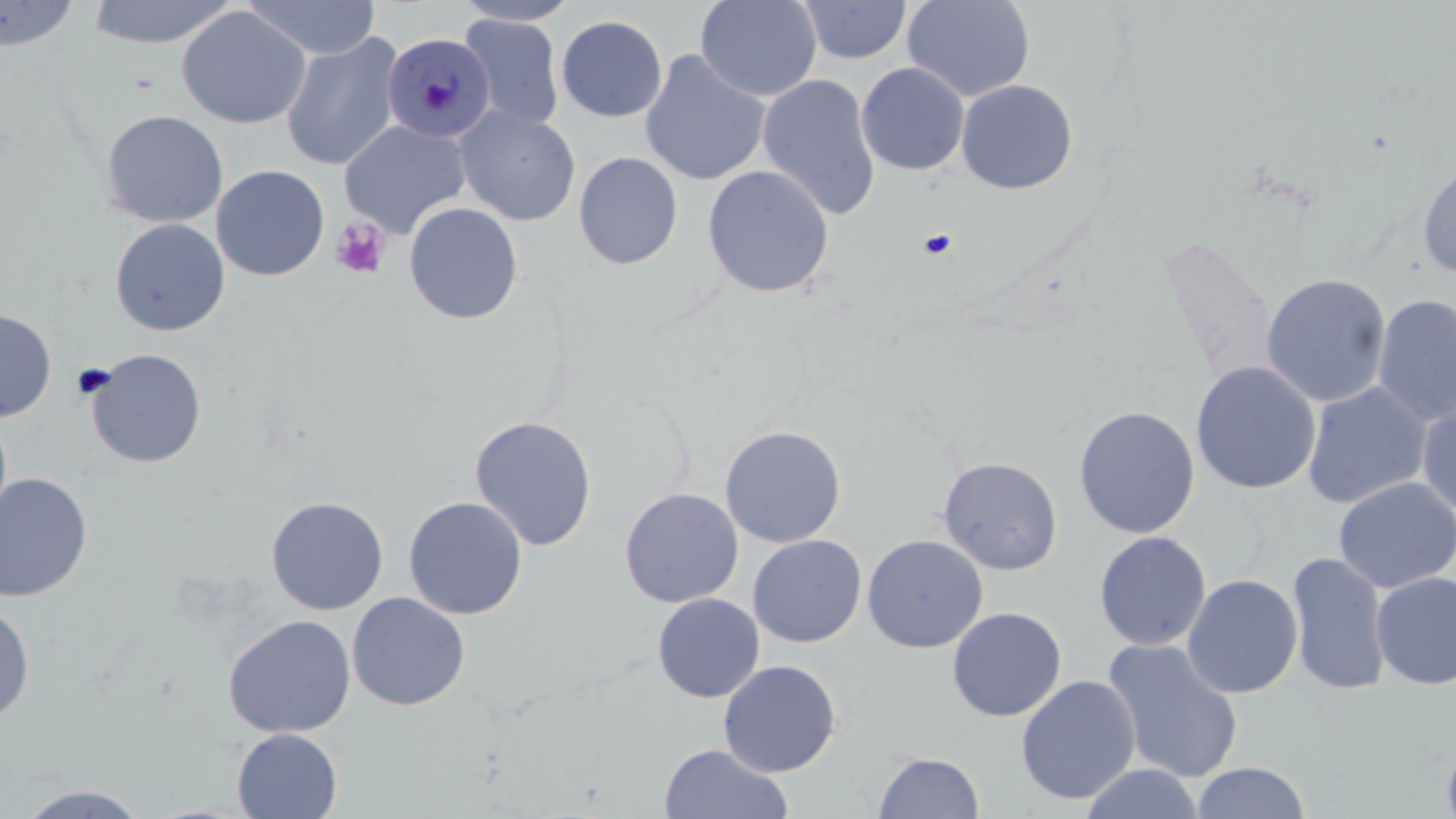
slide-level diagnosis = Plasmodium malariae
uninfected red blood cell locations = approximate bounding boxes as named x1/y1/x2/y2 corners in pixels: (x1=85, y1=0, x2=238, y2=48), (x1=243, y1=0, x2=381, y2=60), (x1=694, y1=0, x2=822, y2=102), (x1=903, y1=0, x2=1035, y2=103), (x1=0, y1=1, x2=81, y2=52), (x1=452, y1=1, x2=581, y2=26), (x1=799, y1=1, x2=912, y2=64), (x1=176, y1=6, x2=311, y2=129), (x1=459, y1=14, x2=566, y2=132), (x1=555, y1=14, x2=668, y2=123), (x1=280, y1=31, x2=404, y2=171), (x1=639, y1=49, x2=770, y2=186), (x1=856, y1=62, x2=970, y2=176), (x1=757, y1=73, x2=881, y2=221), (x1=956, y1=79, x2=1078, y2=195), (x1=455, y1=106, x2=580, y2=226), (x1=99, y1=109, x2=228, y2=228), (x1=338, y1=119, x2=471, y2=238), (x1=573, y1=151, x2=683, y2=270), (x1=1417, y1=155, x2=1456, y2=279), (x1=211, y1=164, x2=330, y2=281), (x1=702, y1=164, x2=835, y2=298), (x1=403, y1=201, x2=523, y2=325), (x1=109, y1=217, x2=230, y2=336), (x1=1155, y1=235, x2=1277, y2=383), (x1=1261, y1=273, x2=1392, y2=408), (x1=1372, y1=293, x2=1456, y2=427), (x1=0, y1=308, x2=56, y2=422), (x1=85, y1=348, x2=207, y2=468), (x1=1190, y1=360, x2=1322, y2=495), (x1=1301, y1=381, x2=1432, y2=509), (x1=1416, y1=397, x2=1456, y2=517), (x1=1073, y1=405, x2=1200, y2=538), (x1=0, y1=408, x2=13, y2=531), (x1=469, y1=415, x2=598, y2=551), (x1=719, y1=424, x2=846, y2=548), (x1=938, y1=456, x2=1063, y2=575), (x1=0, y1=472, x2=93, y2=602), (x1=1333, y1=477, x2=1456, y2=593), (x1=619, y1=487, x2=743, y2=608), (x1=266, y1=496, x2=389, y2=615), (x1=403, y1=496, x2=528, y2=619), (x1=1093, y1=530, x2=1211, y2=651), (x1=747, y1=534, x2=867, y2=648), (x1=862, y1=534, x2=989, y2=653), (x1=1287, y1=551, x2=1392, y2=695), (x1=1371, y1=571, x2=1456, y2=690), (x1=1181, y1=573, x2=1303, y2=699), (x1=347, y1=592, x2=470, y2=710), (x1=652, y1=593, x2=764, y2=703), (x1=1, y1=600, x2=35, y2=726), (x1=946, y1=606, x2=1066, y2=722), (x1=222, y1=614, x2=357, y2=738), (x1=1101, y1=638, x2=1245, y2=783), (x1=718, y1=659, x2=841, y2=777), (x1=1015, y1=674, x2=1141, y2=805), (x1=232, y1=728, x2=342, y2=818), (x1=1440, y1=732, x2=1456, y2=819), (x1=658, y1=743, x2=793, y2=819), (x1=872, y1=751, x2=985, y2=818), (x1=1191, y1=761, x2=1311, y2=819), (x1=1078, y1=763, x2=1207, y2=819), (x1=16, y1=783, x2=151, y2=818)
field of view = one of a larger specimen
stain = May-Grünwald-Giemsa
modality = optical microscopy
platelet locations = approximate bounding boxes as named x1/y1/x2/y2 corners in pixels: (x1=330, y1=217, x2=391, y2=279), (x1=917, y1=229, x2=958, y2=260), (x1=71, y1=363, x2=116, y2=402)
Plasmodium malariae-infected red blood cell locations = approximate bounding boxes as named x1/y1/x2/y2 corners in pixels: (x1=381, y1=32, x2=495, y2=143)
magnification = 1000x
preparation = thin blood smear
image size = 1456×819 pixels